Give the position of every Plasmodium parasite.
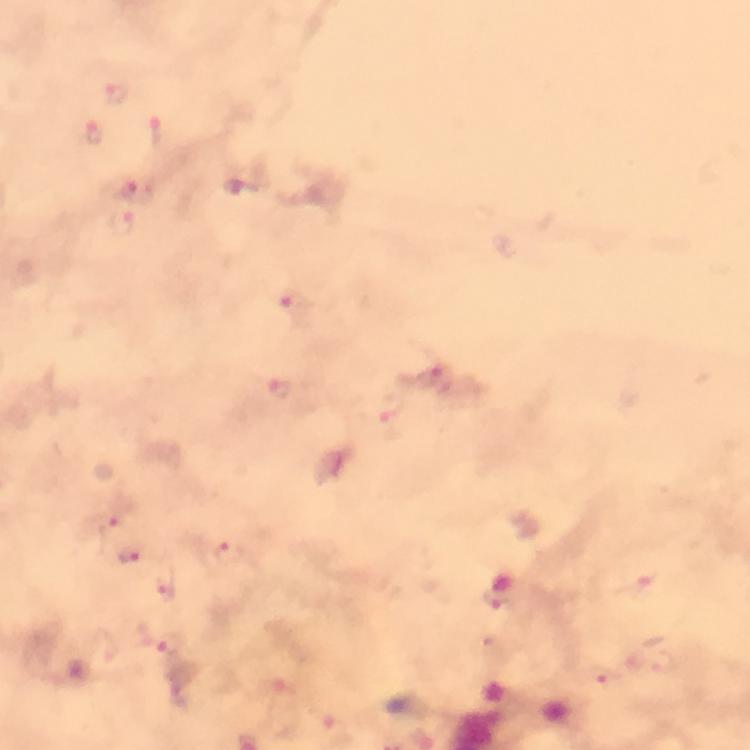
Approximate centers as [x, y] in pixels.
Plasmodium parasites: [117, 95], [94, 133], [156, 133], [138, 191], [124, 225], [293, 305], [441, 380], [281, 389], [394, 409], [106, 522], [228, 552], [132, 555], [166, 586], [499, 597], [164, 642], [608, 679].

At 100x magnification. From a malaria diagnostic workup. Immersion oil was used. Giemsa-stained preparation. Thick blood smear. Cropped region of a single field of view. Image is 750×750 pixels. Smartphone photograph taken through a microscope.